Report the malaria status of this cell.
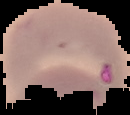

It is parasitized.

Segmented cell region on a black background. Image is 130×115 pixels. From a thin blood smear.